Report the malaria status of this cell.
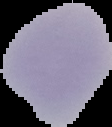
It is uninfected.

Image is 112×127 pixels. The area outside the segmented cell region is set to black. From a thin blood smear.